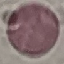
malaria_status: uninfected
image_type: cell patch, automatically extracted from a larger field of view and resized to 64 × 64 pixels
capture: smartphone camera at the microscope eyepiece
stain: Giemsa
preparation: thin blood film